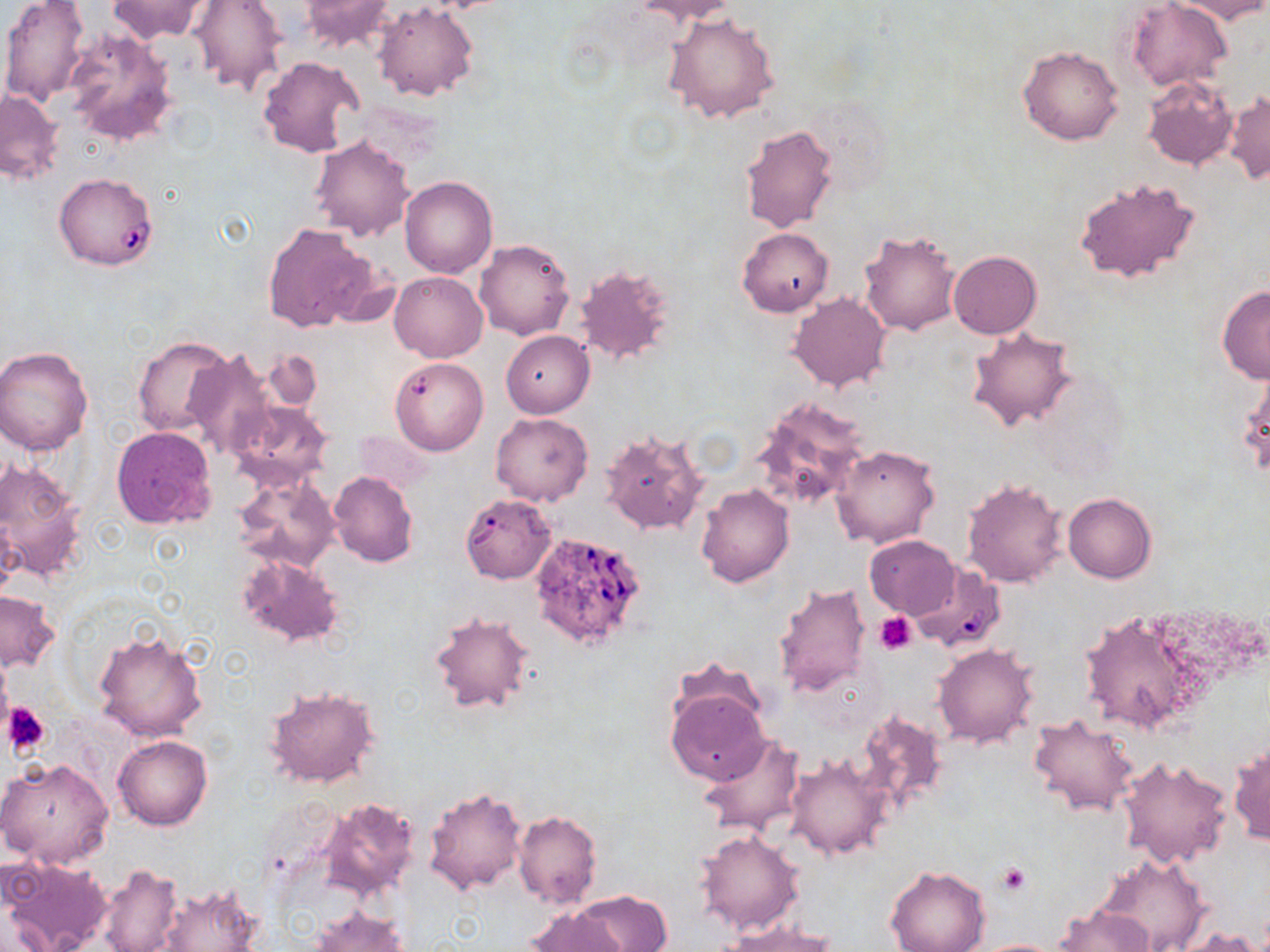
slide-level diagnosis = Babesia divergens
uninfected red blood cell locations = approximate bounding boxes as [x1, y1, x2, y2] in pixels: [1, 0, 89, 105], [108, 0, 214, 43], [632, 0, 739, 24], [1126, 0, 1232, 93], [1171, 0, 1270, 23], [187, 1, 289, 98], [296, 1, 396, 53], [373, 2, 477, 102], [665, 10, 780, 124], [63, 27, 179, 147], [1017, 45, 1123, 146], [257, 54, 365, 159], [1141, 76, 1238, 172], [1226, 89, 1269, 185], [1, 90, 64, 185], [806, 94, 891, 193], [739, 124, 839, 233], [309, 135, 414, 240], [1073, 175, 1201, 286], [400, 176, 497, 278], [262, 223, 381, 333], [739, 228, 833, 316], [859, 228, 962, 335], [474, 239, 574, 340], [949, 251, 1041, 338], [575, 264, 678, 364], [389, 271, 487, 362], [1216, 285, 1270, 384], [788, 293, 890, 394], [966, 326, 1078, 430], [501, 331, 593, 418], [133, 334, 235, 437], [0, 346, 95, 457], [186, 349, 275, 459], [261, 349, 324, 411], [389, 356, 487, 455], [1238, 367, 1270, 479], [749, 398, 870, 513], [228, 401, 335, 492], [491, 412, 593, 505], [111, 425, 218, 529], [599, 428, 709, 536], [830, 443, 940, 550], [0, 458, 89, 585], [328, 471, 418, 567], [234, 472, 339, 572], [961, 477, 1068, 588], [696, 484, 794, 587], [1064, 492, 1157, 581], [463, 497, 558, 584], [864, 536, 960, 618], [236, 553, 346, 649], [907, 560, 1007, 652], [772, 583, 870, 700], [0, 590, 59, 671], [427, 609, 537, 715], [1077, 610, 1201, 734], [93, 628, 208, 743], [933, 644, 1038, 747], [264, 684, 383, 790], [665, 686, 769, 786], [855, 710, 949, 814], [1029, 713, 1140, 818], [699, 732, 806, 835], [114, 735, 211, 830], [1228, 740, 1269, 846], [785, 752, 891, 858], [1117, 757, 1232, 869], [0, 758, 114, 869], [425, 784, 527, 895], [315, 797, 421, 903], [513, 811, 602, 908], [695, 829, 805, 935], [1094, 852, 1209, 952], [0, 856, 112, 952], [98, 863, 184, 952], [885, 866, 991, 952], [154, 881, 260, 952], [572, 891, 671, 951], [309, 906, 409, 952], [524, 906, 629, 952], [1054, 906, 1150, 952], [1173, 923, 1262, 952], [725, 924, 843, 952], [967, 938, 1070, 951]
field of view = single
preparation = thin blood smear
modality = light microscopy
Babesia divergens-infected red blood cell locations = approximate bounding boxes as [x1, y1, x2, y2] in pixels: [62, 182, 158, 272], [529, 530, 647, 650]
magnification = 1000x
platelet locations = approximate bounding boxes as [x1, y1, x2, y2] in pixels: [875, 613, 917, 653], [0, 672, 12, 734], [5, 703, 51, 756], [995, 863, 1031, 895]
stain = May-Grünwald-Giemsa
image size = 1270×952 pixels